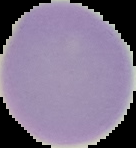

image type = segmented cell region on a black background
preparation = thin blood film
image size = 136×148 pixels
result = no malaria parasites detected